State the blood parasite species.
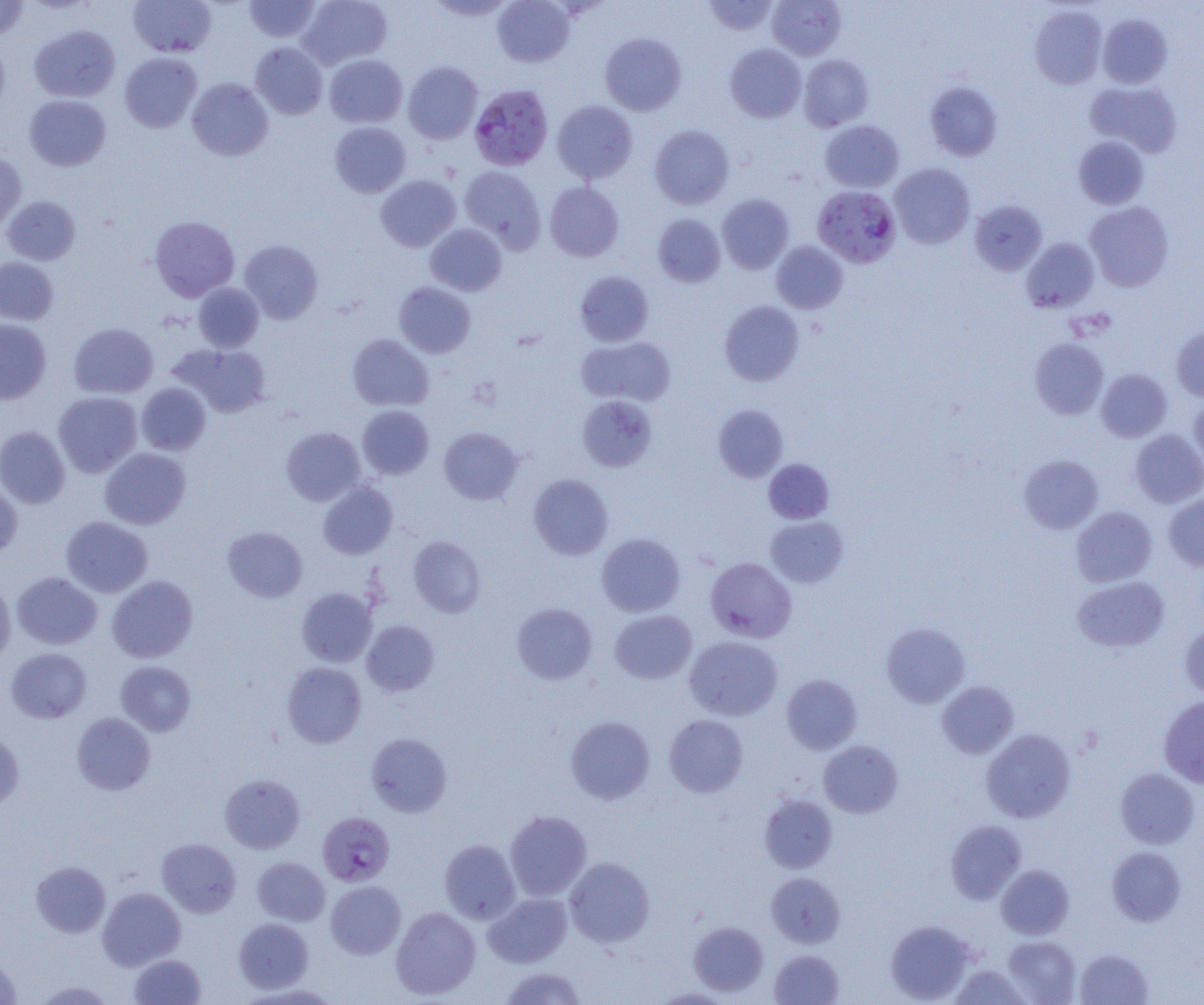
Plasmodium falciparum.

Approximate bounding boxes as named x1/y1/x2/y2 corners in pixels. Uninfected red blood cell locations: (x1=0, y1=0, x2=29, y2=41), (x1=129, y1=0, x2=216, y2=57), (x1=243, y1=0, x2=322, y2=43), (x1=298, y1=0, x2=392, y2=69), (x1=426, y1=0, x2=516, y2=21), (x1=492, y1=0, x2=575, y2=67), (x1=703, y1=0, x2=779, y2=35), (x1=767, y1=0, x2=846, y2=60), (x1=1029, y1=5, x2=1107, y2=89), (x1=1098, y1=14, x2=1172, y2=88), (x1=30, y1=24, x2=119, y2=102), (x1=600, y1=33, x2=686, y2=116), (x1=0, y1=38, x2=9, y2=119), (x1=251, y1=42, x2=327, y2=119), (x1=725, y1=44, x2=806, y2=123), (x1=120, y1=53, x2=203, y2=133), (x1=324, y1=54, x2=407, y2=128), (x1=799, y1=54, x2=873, y2=131), (x1=403, y1=61, x2=483, y2=144), (x1=187, y1=77, x2=273, y2=161), (x1=925, y1=81, x2=1002, y2=161), (x1=1085, y1=81, x2=1182, y2=158), (x1=24, y1=94, x2=111, y2=171), (x1=552, y1=100, x2=638, y2=183), (x1=820, y1=120, x2=904, y2=192), (x1=329, y1=121, x2=411, y2=197), (x1=649, y1=125, x2=735, y2=209), (x1=1073, y1=136, x2=1149, y2=210), (x1=0, y1=152, x2=26, y2=230), (x1=889, y1=163, x2=975, y2=249), (x1=459, y1=166, x2=546, y2=252), (x1=376, y1=175, x2=460, y2=251), (x1=545, y1=181, x2=624, y2=262), (x1=717, y1=194, x2=794, y2=274), (x1=2, y1=196, x2=81, y2=265), (x1=969, y1=200, x2=1047, y2=276), (x1=1085, y1=202, x2=1173, y2=292), (x1=653, y1=214, x2=726, y2=287), (x1=150, y1=216, x2=239, y2=301), (x1=425, y1=224, x2=506, y2=296), (x1=1021, y1=238, x2=1099, y2=313), (x1=239, y1=239, x2=323, y2=324), (x1=771, y1=241, x2=848, y2=313), (x1=0, y1=257, x2=58, y2=325), (x1=575, y1=271, x2=654, y2=347), (x1=193, y1=282, x2=264, y2=352), (x1=394, y1=282, x2=476, y2=358), (x1=719, y1=300, x2=804, y2=386), (x1=0, y1=319, x2=52, y2=405), (x1=69, y1=323, x2=158, y2=398), (x1=1171, y1=326, x2=1204, y2=401), (x1=347, y1=334, x2=434, y2=411), (x1=576, y1=336, x2=676, y2=407), (x1=1030, y1=338, x2=1109, y2=419), (x1=170, y1=343, x2=271, y2=417), (x1=1096, y1=368, x2=1172, y2=442), (x1=137, y1=383, x2=211, y2=455), (x1=53, y1=391, x2=142, y2=477), (x1=578, y1=395, x2=657, y2=472), (x1=1189, y1=398, x2=1204, y2=474), (x1=713, y1=404, x2=788, y2=482), (x1=357, y1=405, x2=434, y2=479), (x1=0, y1=426, x2=70, y2=509), (x1=281, y1=426, x2=365, y2=506), (x1=438, y1=427, x2=523, y2=505), (x1=1131, y1=429, x2=1204, y2=508), (x1=99, y1=448, x2=191, y2=529), (x1=1018, y1=454, x2=1103, y2=534), (x1=763, y1=459, x2=833, y2=523), (x1=529, y1=474, x2=613, y2=560), (x1=317, y1=481, x2=397, y2=559), (x1=0, y1=482, x2=22, y2=558), (x1=1163, y1=493, x2=1204, y2=571), (x1=1071, y1=506, x2=1157, y2=587), (x1=61, y1=516, x2=153, y2=597), (x1=765, y1=516, x2=848, y2=587), (x1=223, y1=526, x2=307, y2=602), (x1=597, y1=533, x2=685, y2=616), (x1=408, y1=535, x2=486, y2=618), (x1=705, y1=557, x2=797, y2=642), (x1=12, y1=572, x2=102, y2=649), (x1=107, y1=575, x2=198, y2=663), (x1=1072, y1=576, x2=1169, y2=653), (x1=0, y1=582, x2=15, y2=666), (x1=296, y1=588, x2=377, y2=667), (x1=511, y1=602, x2=597, y2=685), (x1=609, y1=609, x2=697, y2=684), (x1=361, y1=620, x2=440, y2=697), (x1=1180, y1=620, x2=1204, y2=700), (x1=881, y1=622, x2=970, y2=707), (x1=685, y1=636, x2=783, y2=720), (x1=5, y1=647, x2=91, y2=723), (x1=115, y1=661, x2=196, y2=736), (x1=282, y1=662, x2=367, y2=748), (x1=782, y1=674, x2=862, y2=754), (x1=937, y1=681, x2=1018, y2=759), (x1=1159, y1=695, x2=1204, y2=788), (x1=71, y1=713, x2=155, y2=795), (x1=664, y1=714, x2=748, y2=797), (x1=566, y1=716, x2=655, y2=804), (x1=981, y1=729, x2=1075, y2=822), (x1=0, y1=731, x2=24, y2=812), (x1=366, y1=733, x2=452, y2=816), (x1=818, y1=740, x2=903, y2=818), (x1=1115, y1=768, x2=1199, y2=849), (x1=220, y1=773, x2=305, y2=854), (x1=759, y1=795, x2=838, y2=873), (x1=504, y1=810, x2=592, y2=901), (x1=945, y1=820, x2=1027, y2=904), (x1=156, y1=838, x2=241, y2=917), (x1=439, y1=839, x2=520, y2=923), (x1=1106, y1=846, x2=1186, y2=926), (x1=252, y1=857, x2=330, y2=926), (x1=564, y1=857, x2=655, y2=947), (x1=31, y1=860, x2=111, y2=938), (x1=996, y1=864, x2=1074, y2=939), (x1=766, y1=872, x2=846, y2=948), (x1=325, y1=880, x2=406, y2=959), (x1=98, y1=887, x2=186, y2=970), (x1=484, y1=893, x2=572, y2=968), (x1=391, y1=906, x2=480, y2=999), (x1=234, y1=918, x2=314, y2=993), (x1=885, y1=919, x2=975, y2=1003), (x1=689, y1=921, x2=768, y2=996), (x1=1003, y1=936, x2=1080, y2=1004), (x1=1074, y1=948, x2=1153, y2=1005), (x1=769, y1=949, x2=844, y2=1005), (x1=129, y1=954, x2=206, y2=1005), (x1=0, y1=955, x2=22, y2=1004), (x1=951, y1=963, x2=1031, y2=1005), (x1=498, y1=966, x2=589, y2=1005), (x1=32, y1=980, x2=117, y2=1004), (x1=234, y1=983, x2=342, y2=1004), (x1=648, y1=988, x2=737, y2=1004). Plasmodium falciparum-infected red blood cell locations: (x1=469, y1=84, x2=553, y2=171), (x1=812, y1=185, x2=901, y2=269), (x1=317, y1=811, x2=395, y2=886). Captured at 1000x magnification. Optical microscopy. One field of a larger specimen. Image is 1204×1005 pixels. Thin blood smear.